State which parasite is depicted.
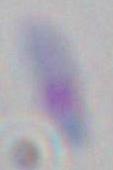

This is Toxoplasma gondii.

modality = photomicrograph
magnification = 1000x